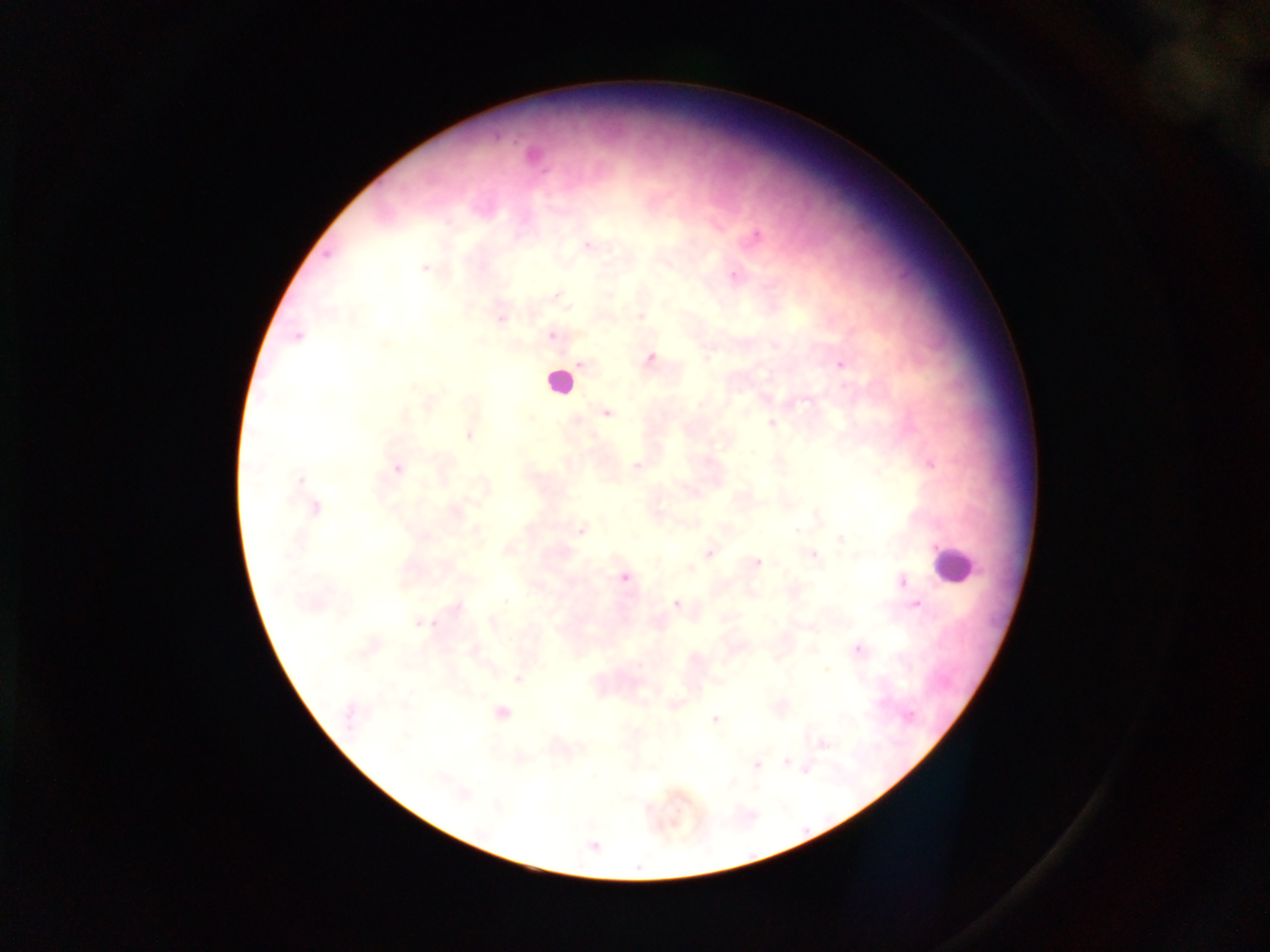
malaria parasite locations = approximate centers as x y in pixels: 533 154; 755 235; 587 246; 425 267; 735 276; 556 296; 499 315; 640 315; 298 335; 552 335; 649 359; 582 363; 841 363; 765 398; 606 413; 772 424; 470 435; 930 463; 636 466; 397 468; 297 481; 314 509; 581 530; 841 538; 508 550; 709 552; 812 554; 756 562; 688 568; 623 577; 900 581; 750 593; 312 603; 677 604; 917 605; 420 623; 856 648; 473 651; 517 678; 674 704; 350 712; 500 713; 715 718; 822 744; 518 758; 787 761; 756 764; 805 768; 591 845
image size = 1270×952 pixels
capture = mobile-phone photograph through a microscope
country = Ghana
field of view = single
leukocyte locations = approximate centers as x y in pixels: 558 382; 952 565
preparation = thick blood film